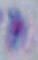
{
  "modality": "photomicrograph",
  "identification": "Toxoplasma gondii",
  "magnification": "1000x"
}